Mark where platelets are.
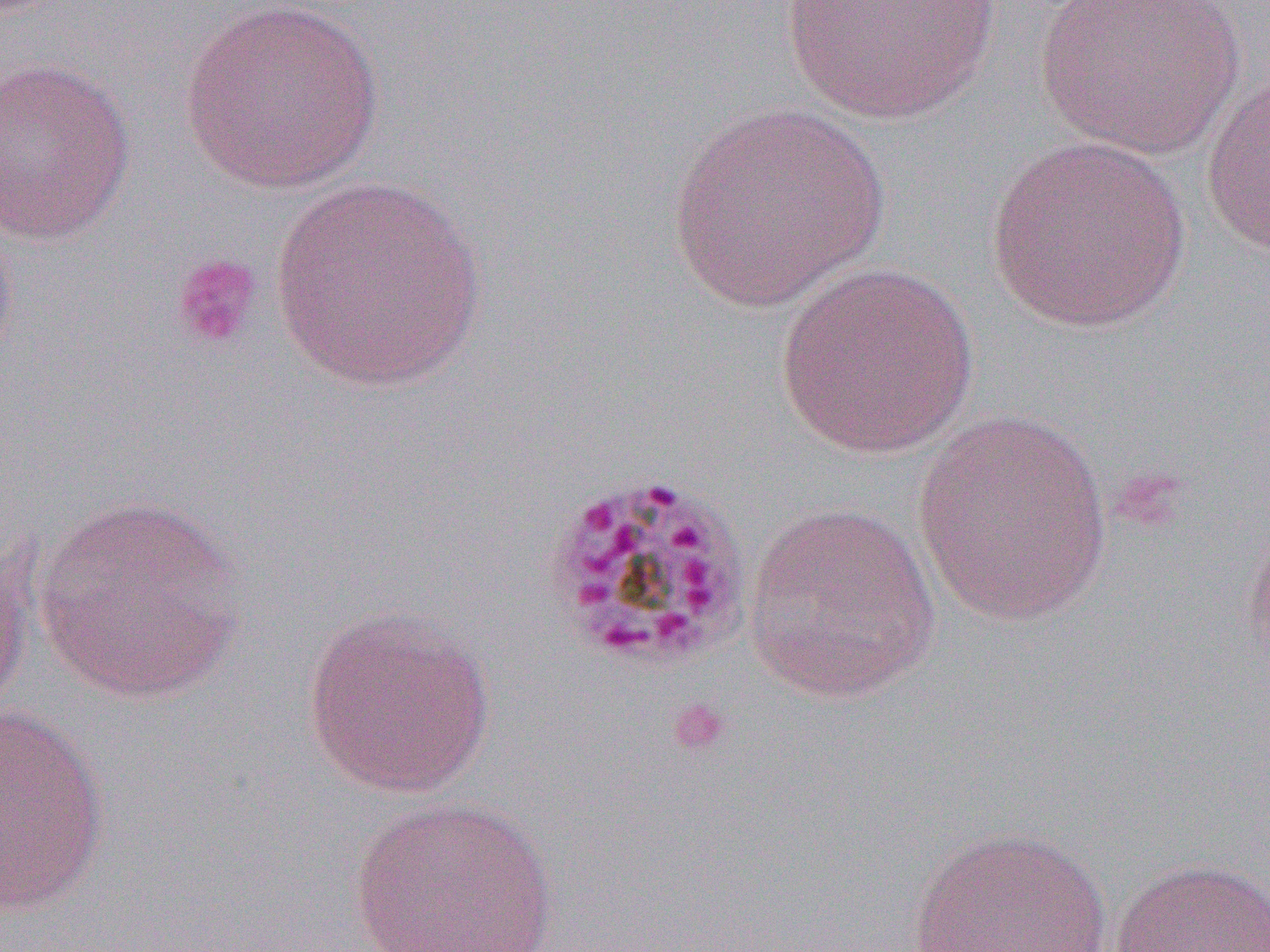

Approximate bounding boxes as [x1, y1, x2, y2] in pixels.
Platelets: [170, 251, 265, 353], [664, 696, 732, 757].

Uninfected red blood cell locations: [178, 0, 385, 196], [1034, 0, 1244, 160], [777, 1, 1002, 124], [0, 56, 137, 245], [1200, 74, 1270, 256], [667, 101, 890, 312], [983, 135, 1192, 333], [270, 176, 489, 390], [0, 210, 20, 379], [776, 261, 978, 458], [910, 411, 1114, 626], [29, 495, 249, 704], [743, 500, 941, 704], [1242, 507, 1270, 686], [0, 529, 35, 727], [301, 606, 497, 799], [0, 704, 111, 916], [345, 794, 562, 952], [905, 826, 1115, 951], [1110, 857, 1269, 951]. Slide-level diagnosis: Plasmodium malariae. Thin blood film. Image is 1270×952 pixels. One field of a larger specimen. Captured at 1000x magnification. Light microscopy.